Assess the morphology of the red blood cells.
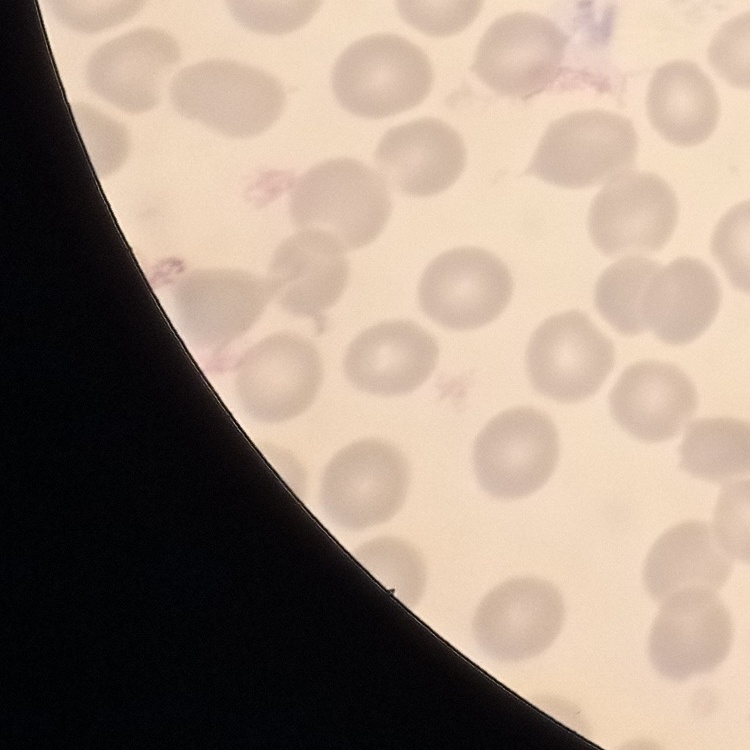
No rouleaux formation.

Summary:
  - Preparation: thin blood film
  - Image type: square crop of a larger photomicrograph
  - Stain: Field's or Giemsa